Classify this cell by malaria status.
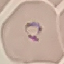

Parasitized.

Acquired by smartphone through the microscope eyepiece. Giemsa-stained preparation. Cell patch, automatically extracted from a larger field of view and resized to 64 × 64 pixels. Thin smear of blood.